Report the malaria status of this cell.
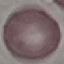
Uninfected.

Thin smear of blood. Giemsa-stained preparation. Cell patch, automatically extracted from a larger field of view and resized to 64 × 64 pixels. Photographed with a smartphone camera at the microscope eyepiece.